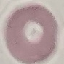

Result: negative for malaria parasites. Giemsa-stained preparation. Photographed with a smartphone camera at the microscope eyepiece. Thin blood smear. Cell patch, automatically extracted from a larger field of view and resized to 64 × 64 pixels.